Outline each blood parasite and name the species.
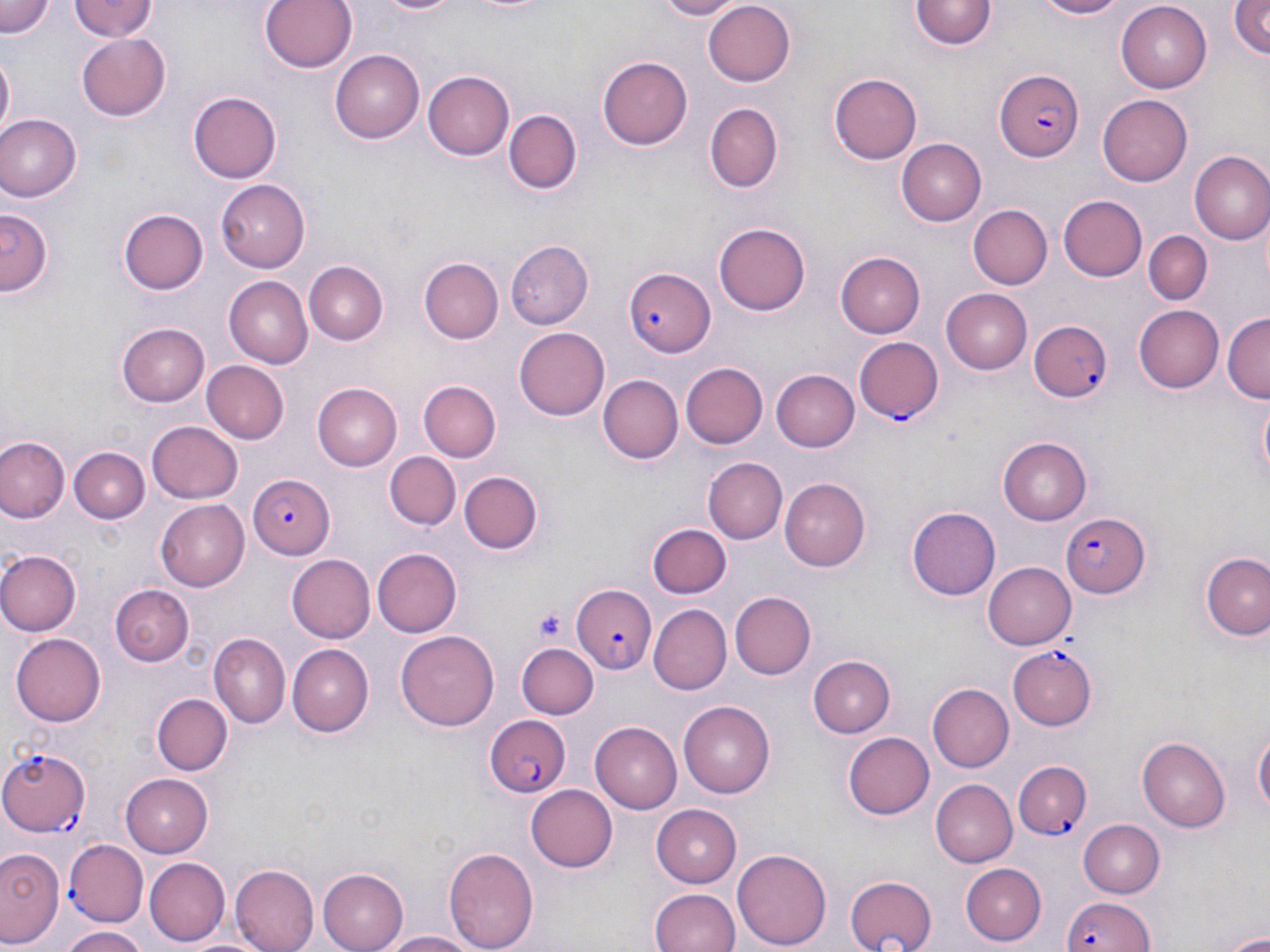

Approximate bounding boxes as (x1, y1, x2, y2) in pixels.
Plasmodium falciparum-infected red blood cells: (993, 68, 1085, 160), (625, 266, 718, 356), (1031, 320, 1116, 401), (854, 337, 944, 427), (248, 476, 335, 559), (1058, 512, 1150, 597), (568, 583, 657, 674), (1009, 646, 1097, 729), (485, 715, 572, 796), (0, 747, 93, 837), (1015, 762, 1090, 838), (63, 840, 146, 927), (1060, 894, 1155, 952).
No Plasmodium ovale, Plasmodium malariae, Plasmodium vivax, Babesia divergens, or Trypanosoma brucei observed.

Summary:
  - Uninfected red blood cell locations: (1, 0, 56, 39), (70, 0, 156, 43), (260, 0, 357, 74), (375, 0, 465, 17), (455, 0, 553, 16), (651, 0, 747, 19), (1025, 0, 1128, 19), (1117, 0, 1212, 89), (1228, 0, 1270, 61), (910, 1, 995, 51), (703, 2, 797, 87), (74, 33, 171, 119), (329, 49, 425, 141), (1, 53, 14, 135), (598, 56, 693, 149), (423, 70, 515, 159), (832, 71, 922, 165), (188, 90, 281, 183), (1097, 95, 1193, 185), (704, 104, 782, 192), (508, 111, 579, 195), (0, 114, 79, 200), (898, 139, 986, 225), (1189, 151, 1270, 245), (217, 179, 310, 272), (1058, 193, 1148, 279), (968, 204, 1052, 290), (1, 209, 50, 298), (119, 209, 208, 295), (713, 222, 813, 315), (1144, 231, 1212, 305), (503, 240, 592, 330), (835, 251, 925, 337), (419, 257, 502, 342), (302, 260, 386, 346), (225, 276, 313, 369), (941, 288, 1032, 373), (1134, 304, 1224, 393), (1223, 314, 1269, 404), (118, 322, 209, 406), (514, 327, 609, 421), (202, 360, 291, 445), (679, 361, 767, 449), (772, 367, 860, 449), (598, 374, 684, 464), (420, 381, 499, 461), (311, 383, 401, 470), (1256, 394, 1269, 490), (149, 420, 243, 502), (1, 437, 69, 522), (997, 437, 1094, 525), (69, 448, 147, 523), (383, 450, 459, 529), (704, 457, 786, 544), (459, 471, 545, 555), (781, 477, 873, 571), (155, 499, 249, 590), (907, 506, 1001, 599), (648, 523, 732, 599), (373, 547, 462, 637), (0, 550, 80, 637), (1204, 553, 1270, 642), (286, 554, 375, 642), (984, 561, 1076, 649), (110, 582, 195, 667), (728, 591, 814, 679), (649, 602, 731, 692), (395, 629, 500, 731), (10, 633, 105, 727), (209, 633, 289, 729), (286, 643, 372, 738), (518, 644, 598, 719), (808, 653, 894, 735), (928, 683, 1015, 772), (153, 694, 231, 775), (678, 701, 775, 798), (593, 721, 686, 813), (1253, 726, 1269, 824), (843, 731, 934, 819), (1137, 737, 1229, 832), (121, 773, 212, 855), (930, 779, 1017, 867), (527, 783, 618, 873), (649, 803, 740, 888), (1076, 818, 1163, 898), (444, 844, 538, 952), (734, 846, 831, 950), (0, 847, 61, 946), (143, 857, 230, 946), (961, 863, 1046, 944), (230, 865, 320, 952), (314, 866, 408, 952), (846, 872, 940, 952), (648, 886, 740, 952), (58, 926, 151, 952), (379, 930, 477, 952), (1222, 930, 1270, 950)
  - Platelet locations: (532, 606, 570, 645)
  - Slide-level diagnosis: Plasmodium falciparum
  - Stain: May-Grünwald-Giemsa
  - Field of view: single
  - Image size: 1270×952 pixels
  - Modality: light microscopy
  - Magnification: 1000x
  - Preparation: thin blood smear